Point out each Plasmodium parasite.
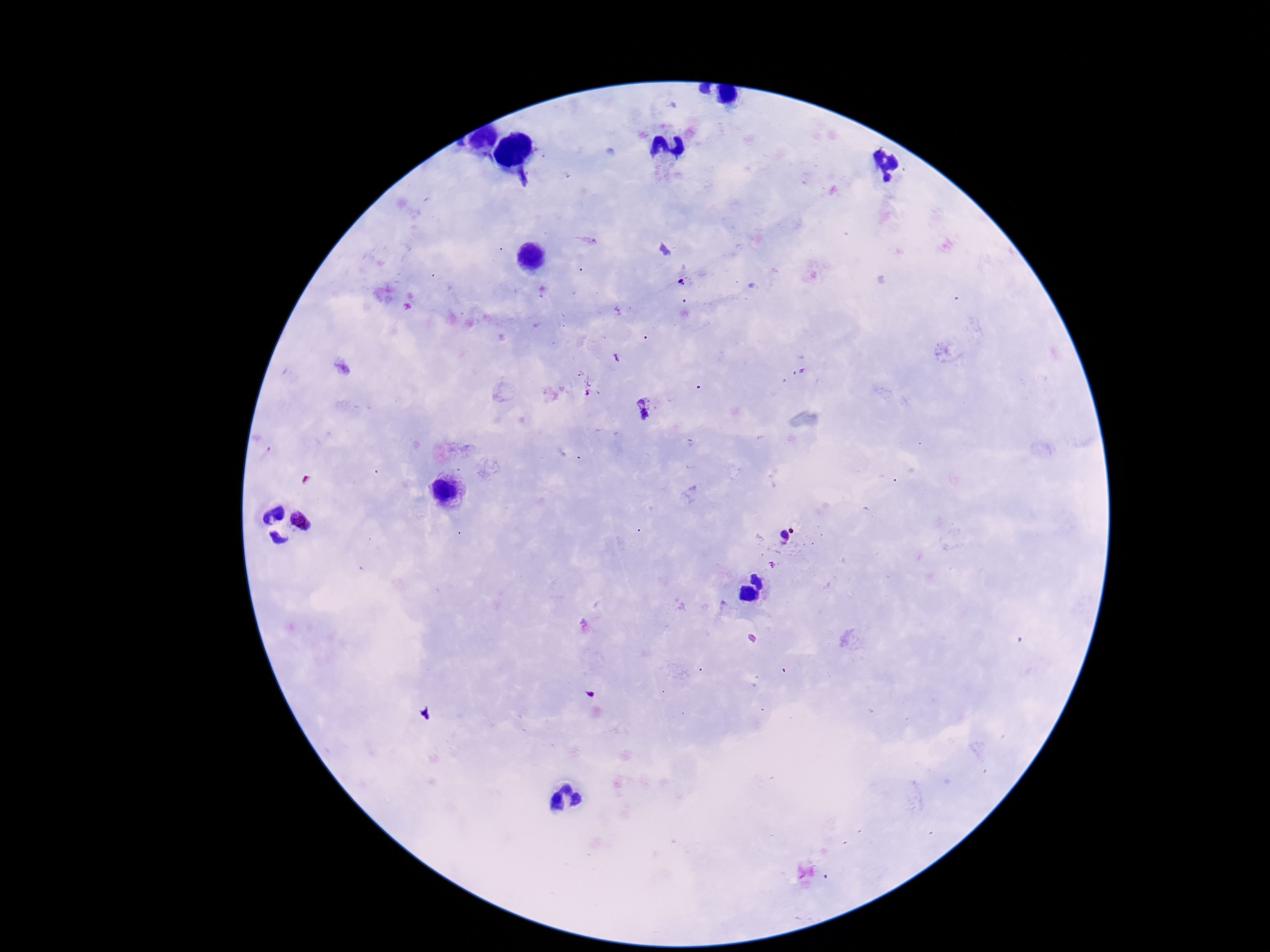

Approximate centers as {x, y} in pixels.
Plasmodium parasites: {681, 282}, {645, 410}, {300, 522}, {788, 535}.

field of view = one from this slide
patient malaria status = infected
image size = 1270×952 pixels
magnification = 100x
capture = smartphone camera through the microscope eyepiece
preparation = thick peripheral-blood smear
stain = Giemsa